Assess the background quality.
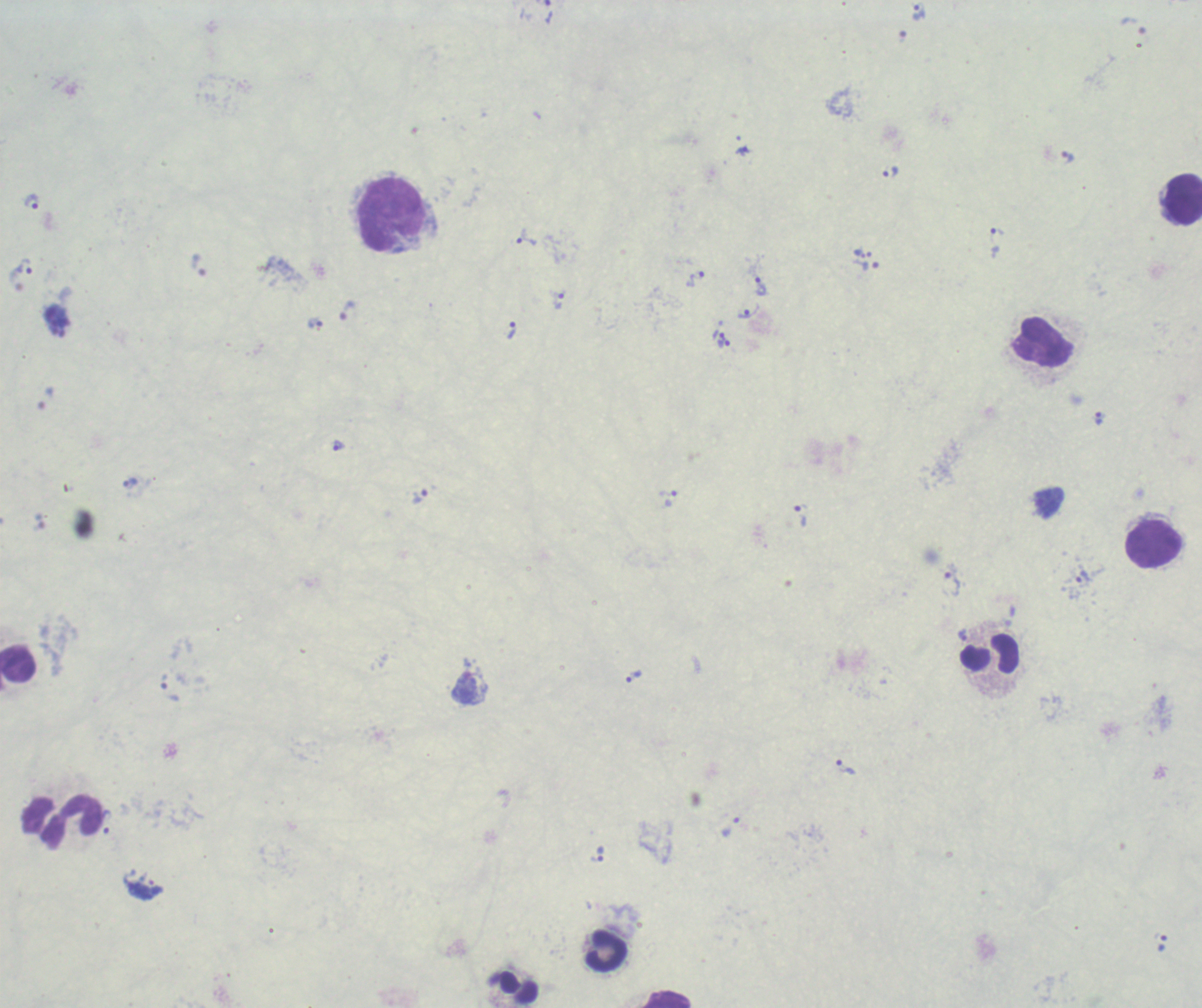

It is poor.

leukocyte_locations: 'approximate centers as (x, y) in pixels: (1183, 198), (392, 214), (1043, 343), (1154, 545), (989, 655), (19, 667), (62, 822), (606, 950), (518, 987), (666, 999)'
result: malaria parasites identified
trophozoite_locations: 'approximate centers as (x, y) in pixels: (919, 11), (742, 151), (1067, 157), (890, 173), (32, 202), (997, 236), (526, 238), (858, 253), (198, 265), (25, 266), (870, 266), (695, 279), (760, 286), (559, 301), (347, 310), (747, 311), (315, 323), (511, 329), (718, 333), (724, 343), (338, 445), (131, 482), (667, 492), (418, 496), (800, 517), (1083, 580), (952, 584), (634, 676), (164, 681), (846, 766), (107, 822), (730, 827), (597, 853)'
field_of_view: one from this slide
stain: Romanowsky
preparation: thick blood film
context: previously used in an actual diagnosis
magnification: 100x
image_size: 1202×1008 pixels